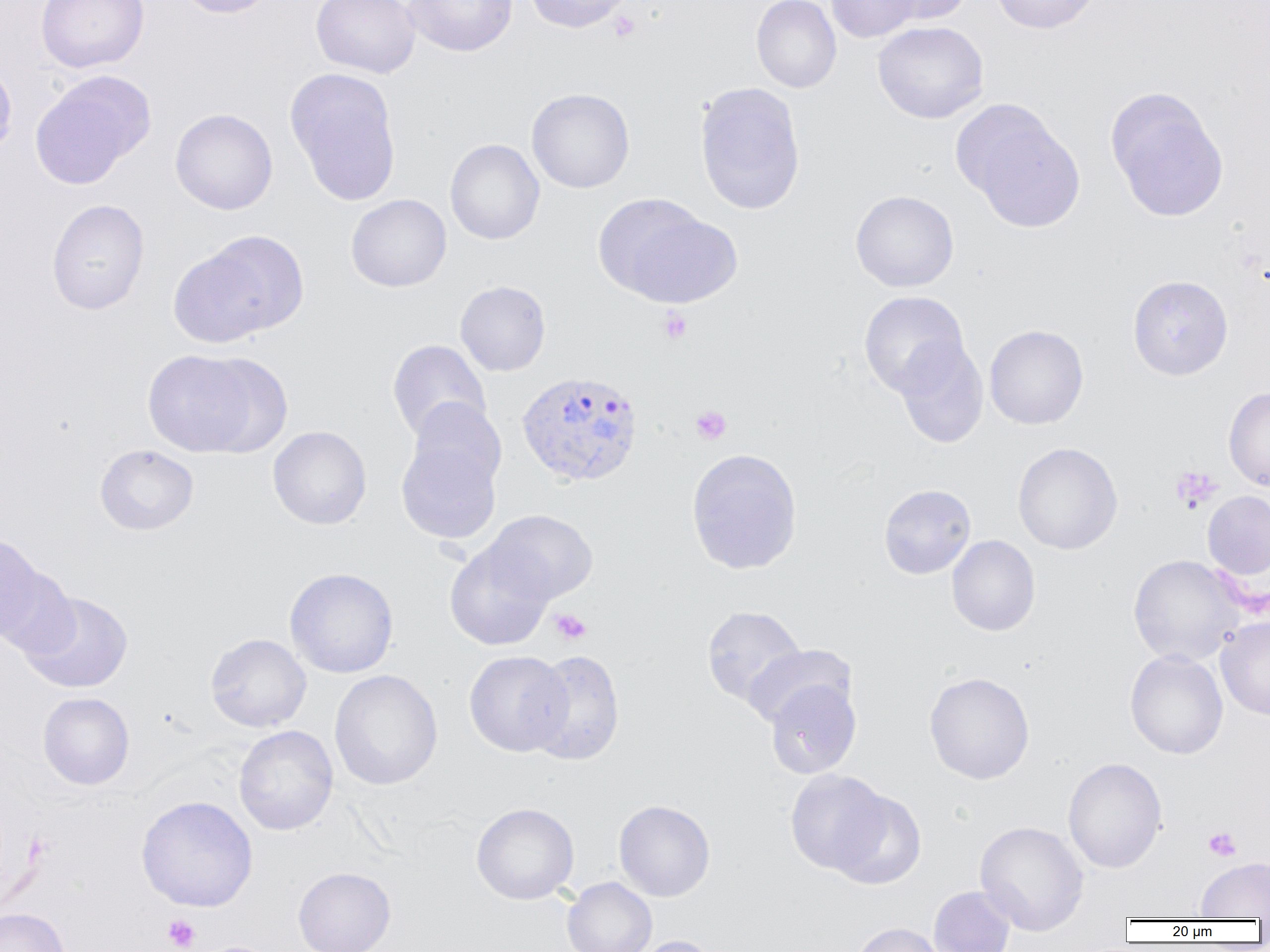
Summary:
  - Coordinate format: approximate bounding boxes as (x1,y1)-(x2,y2) corner pairs in pixels
  - Uninfected red blood cell locations: (36,0)-(149,73), (175,0)-(277,18), (311,0)-(420,78), (403,0)-(518,57), (523,0)-(635,33), (751,0)-(841,93), (826,0)-(924,43), (876,0)-(973,25), (991,0)-(1102,34), (872,20)-(989,124), (0,57)-(18,161), (285,68)-(403,206), (30,72)-(154,189), (694,81)-(806,215), (526,87)-(635,193), (1105,87)-(1229,222), (955,101)-(1085,233), (170,108)-(278,215), (445,139)-(545,245), (850,189)-(959,292), (346,193)-(452,292), (594,194)-(738,307), (46,199)-(149,315), (175,233)-(306,343), (1127,274)-(1233,380), (455,280)-(551,376), (858,291)-(969,397), (984,324)-(1089,430), (387,339)-(492,443), (895,340)-(989,448), (142,349)-(260,456), (195,353)-(294,457), (1223,386)-(1270,491), (407,399)-(507,493), (267,426)-(371,530), (396,435)-(503,544), (1012,442)-(1123,555), (94,444)-(199,535), (686,448)-(803,575), (878,484)-(976,579), (1202,491)-(1270,581), (484,509)-(597,604), (0,533)-(48,645), (947,535)-(1041,636), (444,539)-(554,651), (1128,554)-(1243,666), (284,567)-(399,678), (19,591)-(134,693), (701,605)-(806,709), (1216,616)-(1270,720), (205,633)-(311,732), (742,643)-(856,730), (525,649)-(625,766), (1125,649)-(1228,759), (464,650)-(572,756), (329,669)-(443,790), (924,671)-(1035,784), (764,678)-(861,779), (37,692)-(135,790), (233,724)-(338,835), (1062,757)-(1168,873), (784,769)-(892,875), (829,788)-(927,889), (136,795)-(258,911), (614,800)-(715,901), (471,802)-(579,905), (974,820)-(1089,936), (1196,856)-(1269,919), (292,866)-(396,952), (562,877)-(657,952), (928,885)-(1016,952), (0,907)-(70,952), (850,921)-(949,952), (627,935)-(721,952)
  - Platelet locations: (608,10)-(641,42), (658,307)-(692,344), (691,405)-(732,445), (1169,465)-(1222,513), (549,608)-(592,645), (1203,826)-(1242,862), (163,914)-(200,951)
  - Plasmodium vivax-infected red blood cell locations: (516,370)-(644,487)
  - Slide-level diagnosis: Plasmodium vivax
  - Preparation: thin blood smear
  - Image size: 1270×952 pixels
  - Magnification: 1000x
  - Field of view: single
  - Modality: optical microscopy